State the preparation type.
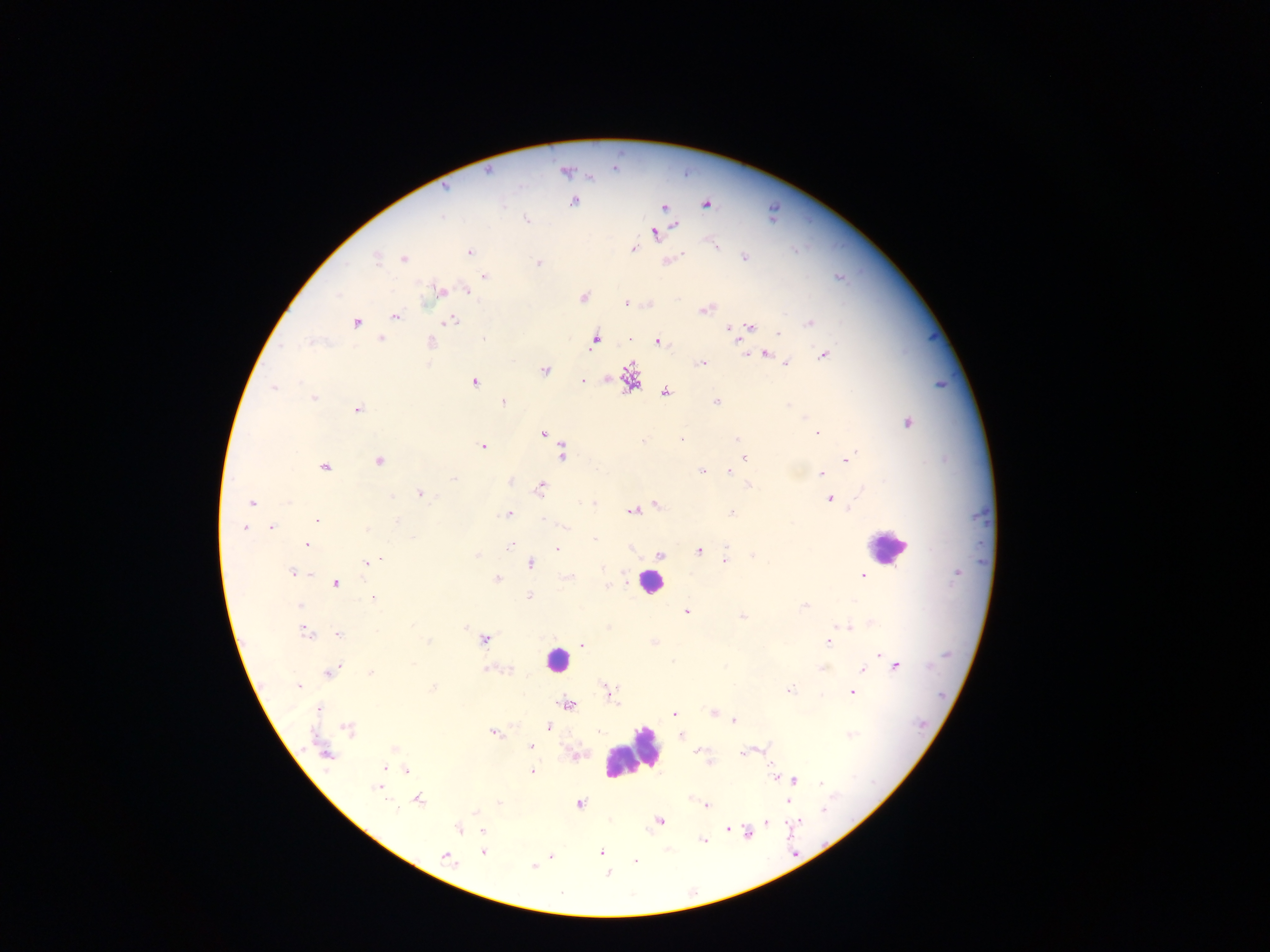
Thick blood smear.

Approximate centers as x y in pixels.
Summary:
  - Malaria parasite locations: 488 172; 565 172; 445 188; 573 201; 705 205; 663 207; 442 216; 526 219; 676 226; 655 234; 715 246; 634 249; 470 252; 376 257; 744 257; 403 258; 673 259; 539 262; 483 276; 839 277; 466 291; 441 292; 583 298; 626 303; 704 309; 395 316; 451 321; 356 323; 809 323; 750 326; 729 329; 778 335; 381 339; 483 339; 595 341; 737 341; 311 342; 657 342; 432 344; 767 354; 824 355; 701 363; 787 363; 544 371; 630 377; 582 381; 299 382; 475 382; 274 388; 665 391; 314 398; 716 401; 503 402; 788 406; 358 409; 907 423; 542 433; 817 434; 682 438; 737 438; 482 446; 742 451; 562 452; 744 457; 848 459; 379 462; 323 467; 702 471; 729 472; 821 474; 454 479; 748 485; 540 487; 420 493; 830 499; 252 503; 593 503; 657 504; 633 510; 732 513; 507 514; 543 519; 318 521; 397 521; 565 525; 271 527; 243 529; 367 530; 594 538; 307 545; 510 546; 557 549; 699 550; 660 555; 477 556; 753 556; 378 560; 725 561; 367 564; 530 564; 603 569; 292 573; 862 576; 496 579; 336 584; 607 585; 529 596; 375 598; 300 605; 805 605; 687 612; 741 617; 846 627; 465 628; 304 633; 339 635; 834 637; 485 639; 428 642; 654 642; 829 642; 582 644; 880 655; 672 662; 896 665; 822 668; 487 670; 507 670; 864 670; 331 672; 370 672; 298 686; 432 689; 790 690; 608 692; 851 692; 568 704; 318 709; 712 713; 675 714; 734 720; 548 726; 348 728; 493 732; 681 734; 850 734; 532 746; 697 750; 743 752; 326 755; 709 762; 384 767; 407 770; 532 772; 774 777; 795 780; 821 784; 377 787; 418 799; 788 801; 499 803; 579 804; 707 806; 823 810; 475 812; 660 821; 766 822; 798 822; 456 828; 727 828; 482 831; 747 833; 702 841; 668 850; 483 852; 601 853; 446 857; 551 857; 634 861; 534 867; 608 873
  - Leukocyte locations: 889 546; 649 582; 557 661; 632 753
  - Image size: 1270×952 pixels
  - Country: Ghana
  - Capture: mobile-phone photograph through a microscope
  - Field of view: single